Give the position of every Plasmodium parasite visible.
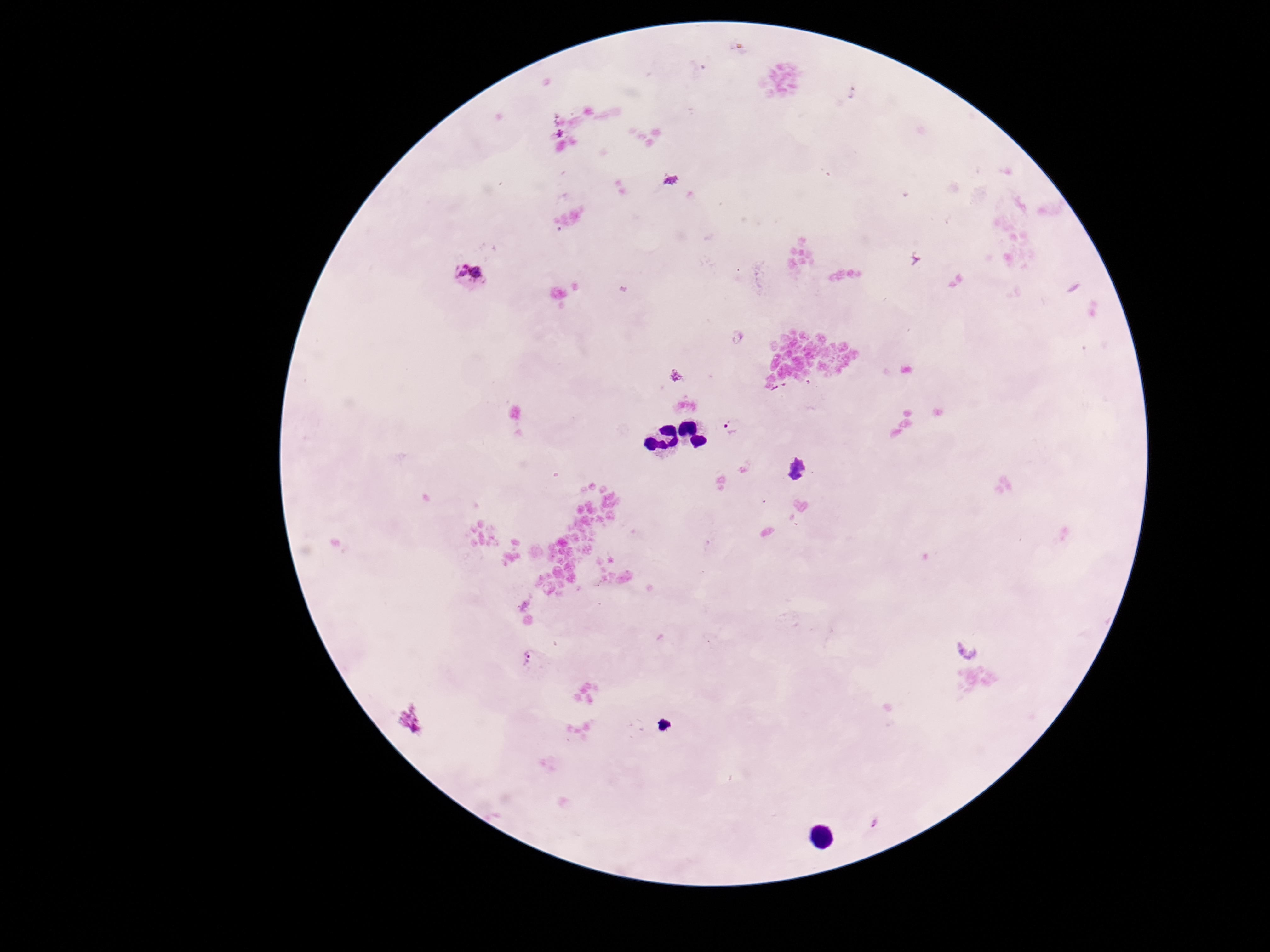

Approximate centers as (x, y) in pixels.
Plasmodium parasites: (670, 181), (469, 273), (676, 377), (733, 428), (798, 470), (968, 652), (530, 658), (875, 824).

Summary:
  - Preparation: thick blood smear
  - Field of view: single
  - Capture: smartphone camera through the microscope eyepiece
  - Stain: Giemsa
  - Magnification: 100x
  - Patient malaria status: positive
  - Image size: 1270×952 pixels